Identify the parasite.
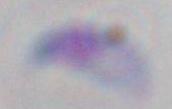

Toxoplasma gondii.

Summary:
  - Magnification: 1000x
  - Modality: micrograph